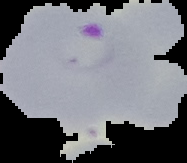
Malaria status: parasitized. Segmented cell region on a black background. From a thin blood film. Image is 187×163 pixels.